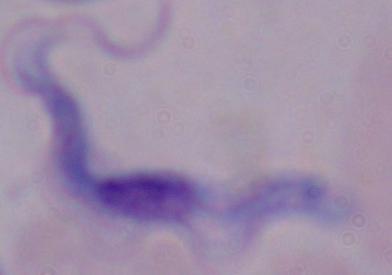
modality = micrograph
magnification = 1000x
identification = trypanosome